State which parasite is depicted.
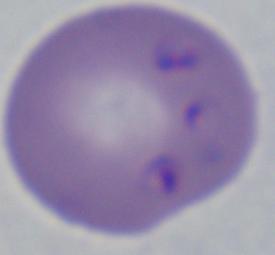
This is Babesia.

magnification = 1000x
modality = micrograph